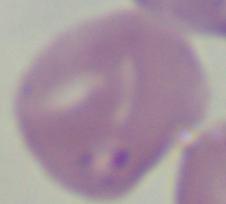
Summary:
  - Magnification: 1000x
  - Identification: Babesia
  - Modality: photomicrograph